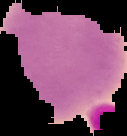
Summary:
  - Image type: cell region segmented out of the field of view; surrounding area masked to black
  - Result: no malaria parasites detected
  - Image size: 127×136 pixels
  - Preparation: thin blood smear